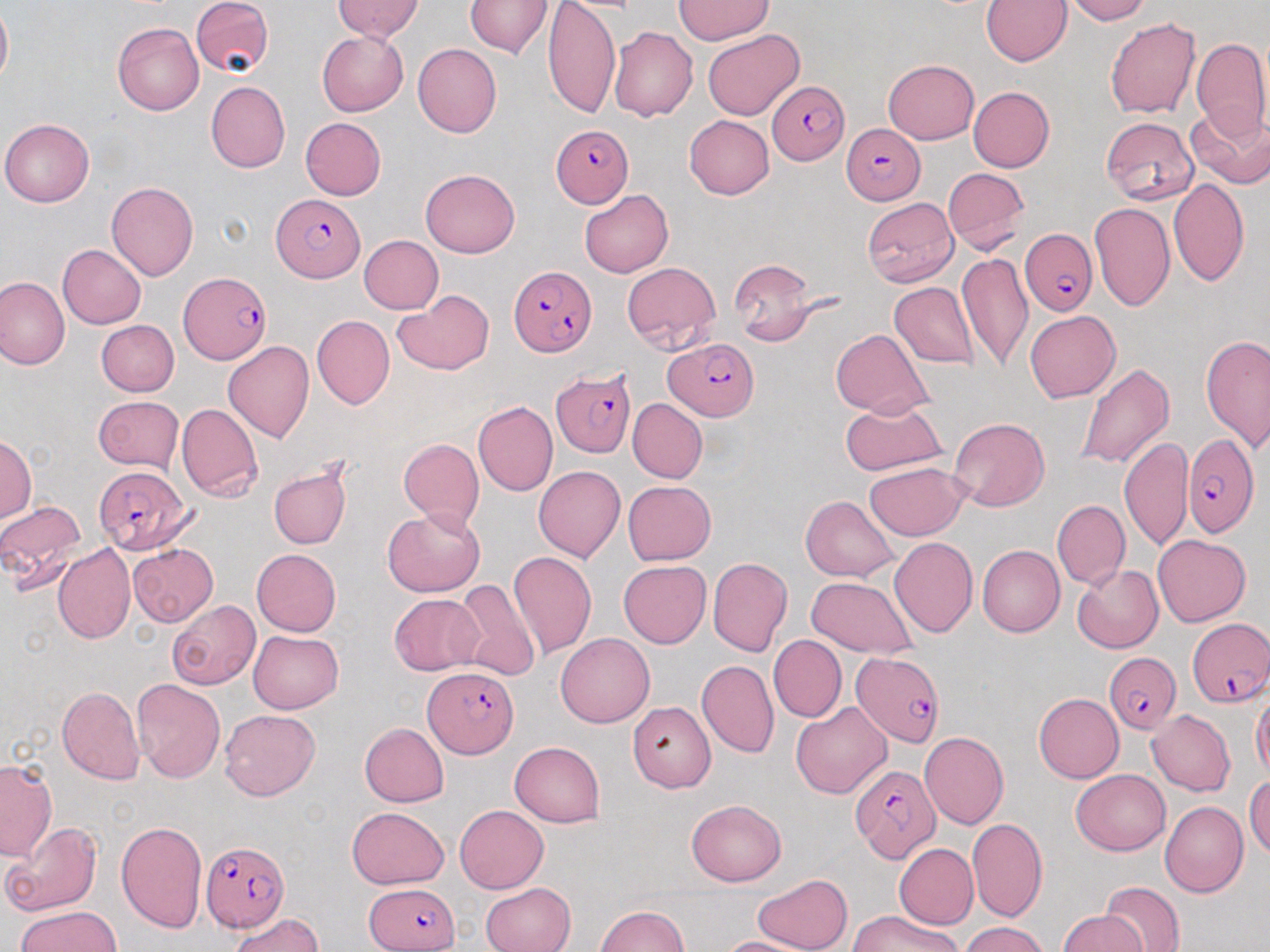
Summary:
  - Coordinate format: approximate bounding boxes as named x1/y1/x2/y2 corners in pixels
  - Uninfected red blood cell locations: (x1=191, y1=0, x2=273, y2=78), (x1=334, y1=0, x2=423, y2=41), (x1=543, y1=0, x2=619, y2=120), (x1=674, y1=0, x2=773, y2=45), (x1=981, y1=0, x2=1072, y2=66), (x1=1062, y1=0, x2=1150, y2=24), (x1=466, y1=1, x2=552, y2=59), (x1=0, y1=3, x2=12, y2=90), (x1=1105, y1=18, x2=1200, y2=119), (x1=112, y1=21, x2=204, y2=115), (x1=609, y1=26, x2=697, y2=121), (x1=703, y1=29, x2=804, y2=121), (x1=316, y1=30, x2=408, y2=116), (x1=1192, y1=37, x2=1270, y2=142), (x1=412, y1=43, x2=502, y2=137), (x1=883, y1=58, x2=979, y2=144), (x1=206, y1=81, x2=290, y2=172), (x1=968, y1=87, x2=1055, y2=172), (x1=1186, y1=104, x2=1270, y2=189), (x1=684, y1=115, x2=774, y2=199), (x1=1100, y1=116, x2=1200, y2=206), (x1=300, y1=117, x2=386, y2=199), (x1=1, y1=118, x2=94, y2=207), (x1=943, y1=167, x2=1029, y2=253), (x1=420, y1=168, x2=520, y2=257), (x1=1168, y1=178, x2=1250, y2=288), (x1=106, y1=181, x2=199, y2=280), (x1=580, y1=189, x2=673, y2=278), (x1=861, y1=197, x2=957, y2=287), (x1=1089, y1=203, x2=1175, y2=313), (x1=360, y1=235, x2=443, y2=313), (x1=56, y1=245, x2=145, y2=329), (x1=958, y1=252, x2=1032, y2=373), (x1=729, y1=260, x2=824, y2=346), (x1=622, y1=262, x2=721, y2=353), (x1=0, y1=275, x2=69, y2=370), (x1=889, y1=282, x2=978, y2=369), (x1=393, y1=290, x2=494, y2=376), (x1=1025, y1=310, x2=1121, y2=402), (x1=312, y1=315, x2=394, y2=408), (x1=97, y1=320, x2=179, y2=397), (x1=831, y1=328, x2=933, y2=418), (x1=1200, y1=334, x2=1270, y2=452), (x1=223, y1=342, x2=315, y2=443), (x1=1073, y1=361, x2=1176, y2=471), (x1=92, y1=396, x2=184, y2=474), (x1=628, y1=398, x2=707, y2=484), (x1=840, y1=399, x2=948, y2=476), (x1=472, y1=401, x2=557, y2=497), (x1=176, y1=403, x2=263, y2=503), (x1=948, y1=417, x2=1048, y2=512), (x1=1120, y1=436, x2=1191, y2=549), (x1=0, y1=437, x2=36, y2=522), (x1=398, y1=438, x2=484, y2=533), (x1=269, y1=462, x2=353, y2=551), (x1=864, y1=462, x2=968, y2=541), (x1=533, y1=465, x2=625, y2=562), (x1=622, y1=481, x2=715, y2=565), (x1=800, y1=494, x2=898, y2=581), (x1=0, y1=499, x2=88, y2=592), (x1=1052, y1=499, x2=1130, y2=590), (x1=383, y1=509, x2=484, y2=596), (x1=1152, y1=533, x2=1251, y2=627), (x1=889, y1=537, x2=977, y2=638), (x1=52, y1=543, x2=135, y2=643), (x1=129, y1=543, x2=218, y2=626), (x1=977, y1=545, x2=1064, y2=637), (x1=252, y1=548, x2=342, y2=636), (x1=507, y1=550, x2=597, y2=659), (x1=708, y1=557, x2=792, y2=657), (x1=618, y1=561, x2=711, y2=648), (x1=1072, y1=564, x2=1164, y2=653), (x1=806, y1=576, x2=918, y2=658), (x1=451, y1=579, x2=541, y2=681), (x1=389, y1=594, x2=485, y2=675), (x1=166, y1=599, x2=260, y2=690), (x1=248, y1=629, x2=344, y2=714), (x1=556, y1=632, x2=654, y2=727), (x1=768, y1=634, x2=847, y2=723), (x1=696, y1=660, x2=778, y2=758), (x1=133, y1=679, x2=225, y2=783), (x1=57, y1=686, x2=144, y2=785), (x1=1251, y1=691, x2=1270, y2=781), (x1=1034, y1=693, x2=1123, y2=783), (x1=627, y1=701, x2=715, y2=793), (x1=791, y1=701, x2=892, y2=799), (x1=219, y1=709, x2=321, y2=801), (x1=1146, y1=710, x2=1236, y2=795), (x1=359, y1=723, x2=449, y2=807), (x1=919, y1=732, x2=1009, y2=830), (x1=509, y1=742, x2=606, y2=827), (x1=0, y1=759, x2=57, y2=861), (x1=1072, y1=770, x2=1170, y2=855), (x1=1245, y1=777, x2=1270, y2=859), (x1=687, y1=799, x2=786, y2=885), (x1=1161, y1=802, x2=1248, y2=897), (x1=455, y1=805, x2=548, y2=893), (x1=346, y1=807, x2=450, y2=889), (x1=967, y1=818, x2=1048, y2=923), (x1=116, y1=819, x2=208, y2=934), (x1=3, y1=821, x2=103, y2=916), (x1=893, y1=843, x2=979, y2=929), (x1=752, y1=873, x2=852, y2=952), (x1=1099, y1=880, x2=1186, y2=952), (x1=480, y1=882, x2=575, y2=952), (x1=595, y1=905, x2=688, y2=952), (x1=15, y1=906, x2=122, y2=952), (x1=849, y1=909, x2=961, y2=952), (x1=1057, y1=910, x2=1148, y2=952), (x1=228, y1=912, x2=324, y2=952), (x1=959, y1=921, x2=1050, y2=952), (x1=715, y1=936, x2=817, y2=952)
  - Plasmodium falciparum-infected red blood cell locations: (x1=769, y1=81, x2=847, y2=166), (x1=842, y1=123, x2=926, y2=204), (x1=550, y1=124, x2=634, y2=208), (x1=271, y1=194, x2=365, y2=283), (x1=1020, y1=229, x2=1097, y2=316), (x1=510, y1=263, x2=596, y2=356), (x1=178, y1=270, x2=271, y2=366), (x1=666, y1=338, x2=758, y2=420), (x1=550, y1=369, x2=636, y2=458), (x1=1183, y1=434, x2=1259, y2=537), (x1=94, y1=465, x2=194, y2=554), (x1=1188, y1=615, x2=1270, y2=707), (x1=849, y1=652, x2=945, y2=748), (x1=1103, y1=652, x2=1180, y2=734), (x1=424, y1=667, x2=518, y2=757), (x1=850, y1=763, x2=940, y2=864), (x1=204, y1=842, x2=287, y2=929), (x1=365, y1=882, x2=461, y2=952)
  - Slide-level diagnosis: Plasmodium falciparum
  - Magnification: 1000x
  - Field of view: single
  - Modality: light microscopy
  - Image size: 1270×952 pixels
  - Stain: May-Grünwald-Giemsa
  - Preparation: thin blood smear